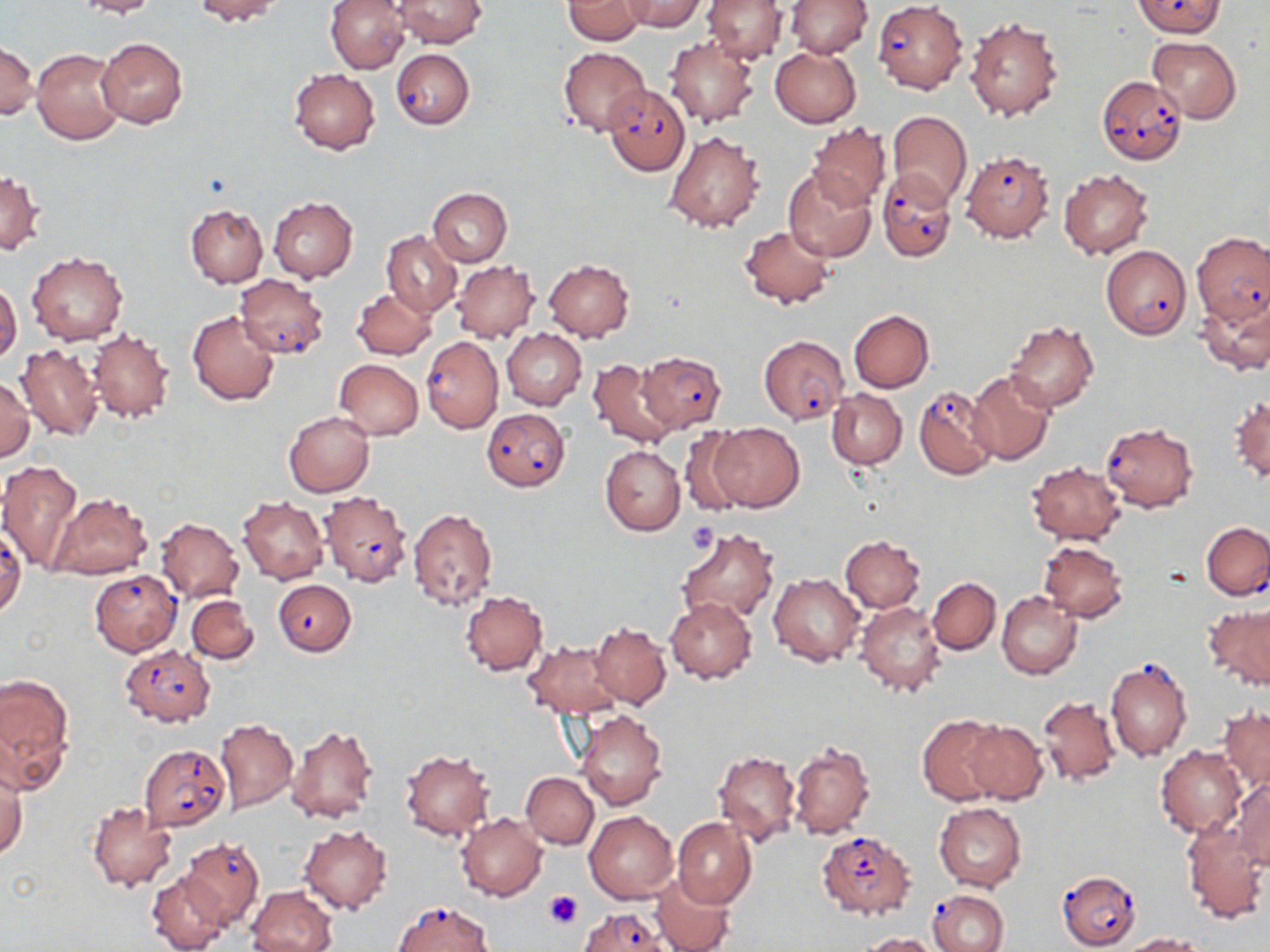
Summary:
  - Coordinate format: approximate bounding boxes as named x1/y1/x2/y2 corners in pixels
  - Platelet locations: (x1=686, y1=522, x2=716, y2=552), (x1=543, y1=890, x2=583, y2=929)
  - Plasmodium falciparum-infected red blood cell locations: (x1=1134, y1=0, x2=1224, y2=37), (x1=872, y1=1, x2=967, y2=93), (x1=390, y1=49, x2=474, y2=130), (x1=1096, y1=76, x2=1188, y2=165), (x1=604, y1=85, x2=690, y2=175), (x1=959, y1=149, x2=1054, y2=242), (x1=877, y1=168, x2=956, y2=264), (x1=1192, y1=232, x2=1270, y2=326), (x1=1101, y1=243, x2=1192, y2=340), (x1=234, y1=275, x2=330, y2=359), (x1=758, y1=335, x2=848, y2=424), (x1=421, y1=336, x2=503, y2=434), (x1=637, y1=350, x2=726, y2=432), (x1=914, y1=384, x2=999, y2=481), (x1=482, y1=408, x2=570, y2=491), (x1=1100, y1=420, x2=1199, y2=513), (x1=318, y1=491, x2=412, y2=586), (x1=1201, y1=522, x2=1270, y2=600), (x1=0, y1=526, x2=26, y2=620), (x1=90, y1=569, x2=181, y2=656), (x1=273, y1=579, x2=355, y2=656), (x1=119, y1=644, x2=214, y2=726), (x1=1105, y1=653, x2=1192, y2=763), (x1=138, y1=744, x2=231, y2=832), (x1=816, y1=831, x2=916, y2=920), (x1=179, y1=838, x2=264, y2=929), (x1=1057, y1=870, x2=1141, y2=950), (x1=928, y1=888, x2=1009, y2=952), (x1=392, y1=900, x2=494, y2=951), (x1=578, y1=907, x2=670, y2=952)
  - Uninfected red blood cell locations: (x1=75, y1=0, x2=160, y2=18), (x1=191, y1=0, x2=282, y2=24), (x1=326, y1=0, x2=410, y2=74), (x1=562, y1=0, x2=645, y2=45), (x1=622, y1=0, x2=705, y2=32), (x1=702, y1=0, x2=787, y2=63), (x1=786, y1=0, x2=872, y2=58), (x1=392, y1=1, x2=486, y2=48), (x1=964, y1=16, x2=1063, y2=122), (x1=96, y1=37, x2=189, y2=128), (x1=663, y1=37, x2=757, y2=127), (x1=1146, y1=37, x2=1242, y2=124), (x1=0, y1=39, x2=38, y2=120), (x1=559, y1=46, x2=650, y2=136), (x1=769, y1=46, x2=862, y2=127), (x1=32, y1=48, x2=126, y2=144), (x1=289, y1=68, x2=380, y2=154), (x1=887, y1=111, x2=972, y2=209), (x1=807, y1=122, x2=892, y2=210), (x1=663, y1=131, x2=764, y2=233), (x1=783, y1=166, x2=878, y2=263), (x1=1059, y1=169, x2=1154, y2=259), (x1=1, y1=170, x2=44, y2=256), (x1=427, y1=188, x2=512, y2=266), (x1=268, y1=197, x2=358, y2=283), (x1=185, y1=205, x2=267, y2=287), (x1=739, y1=224, x2=836, y2=310), (x1=381, y1=231, x2=462, y2=318), (x1=26, y1=250, x2=128, y2=345), (x1=452, y1=259, x2=539, y2=343), (x1=543, y1=259, x2=634, y2=341), (x1=0, y1=281, x2=21, y2=364), (x1=352, y1=288, x2=436, y2=358), (x1=1197, y1=293, x2=1270, y2=376), (x1=849, y1=310, x2=934, y2=392), (x1=188, y1=311, x2=279, y2=405), (x1=1004, y1=320, x2=1098, y2=413), (x1=88, y1=328, x2=176, y2=423), (x1=503, y1=330, x2=585, y2=409), (x1=15, y1=344, x2=102, y2=440), (x1=333, y1=358, x2=422, y2=440), (x1=586, y1=358, x2=681, y2=449), (x1=966, y1=370, x2=1056, y2=465), (x1=1, y1=376, x2=35, y2=461), (x1=827, y1=389, x2=907, y2=468), (x1=1228, y1=396, x2=1269, y2=484), (x1=285, y1=411, x2=374, y2=496), (x1=708, y1=422, x2=804, y2=512), (x1=677, y1=427, x2=759, y2=518), (x1=600, y1=445, x2=685, y2=536), (x1=0, y1=459, x2=83, y2=571), (x1=1025, y1=461, x2=1125, y2=545), (x1=49, y1=493, x2=152, y2=581), (x1=237, y1=497, x2=328, y2=584), (x1=406, y1=509, x2=498, y2=611), (x1=155, y1=517, x2=244, y2=602), (x1=675, y1=527, x2=778, y2=624), (x1=839, y1=536, x2=925, y2=612), (x1=1038, y1=541, x2=1128, y2=621), (x1=769, y1=573, x2=865, y2=666), (x1=927, y1=576, x2=1000, y2=654), (x1=460, y1=590, x2=548, y2=675), (x1=996, y1=591, x2=1081, y2=681), (x1=187, y1=595, x2=259, y2=665), (x1=666, y1=597, x2=756, y2=683), (x1=855, y1=600, x2=944, y2=697), (x1=1203, y1=603, x2=1270, y2=691), (x1=588, y1=622, x2=672, y2=709), (x1=523, y1=639, x2=625, y2=719), (x1=0, y1=672, x2=73, y2=787), (x1=1037, y1=694, x2=1121, y2=788), (x1=1219, y1=706, x2=1269, y2=792), (x1=573, y1=709, x2=668, y2=810), (x1=917, y1=715, x2=1005, y2=805), (x1=216, y1=717, x2=298, y2=812), (x1=964, y1=720, x2=1047, y2=804), (x1=286, y1=724, x2=379, y2=824), (x1=140, y1=729, x2=298, y2=820), (x1=787, y1=742, x2=876, y2=840), (x1=1156, y1=745, x2=1246, y2=835), (x1=400, y1=749, x2=496, y2=841), (x1=712, y1=750, x2=801, y2=846), (x1=1, y1=767, x2=25, y2=859), (x1=521, y1=772, x2=598, y2=849), (x1=1228, y1=779, x2=1270, y2=869), (x1=87, y1=801, x2=178, y2=891), (x1=933, y1=804, x2=1027, y2=890), (x1=584, y1=811, x2=678, y2=903), (x1=456, y1=812, x2=547, y2=901), (x1=672, y1=817, x2=756, y2=908), (x1=1182, y1=821, x2=1268, y2=923), (x1=299, y1=825, x2=392, y2=914), (x1=147, y1=873, x2=228, y2=951), (x1=652, y1=875, x2=732, y2=952), (x1=248, y1=886, x2=337, y2=952), (x1=857, y1=932, x2=942, y2=952), (x1=1123, y1=933, x2=1209, y2=951)
  - Slide-level diagnosis: Plasmodium falciparum
  - Stain: May-Grünwald-Giemsa
  - Preparation: thin blood film
  - Image size: 1270×952 pixels
  - Modality: light microscopy
  - Field of view: one of a larger specimen
  - Magnification: 1000x